Comment on the morphology of the red blood cells.
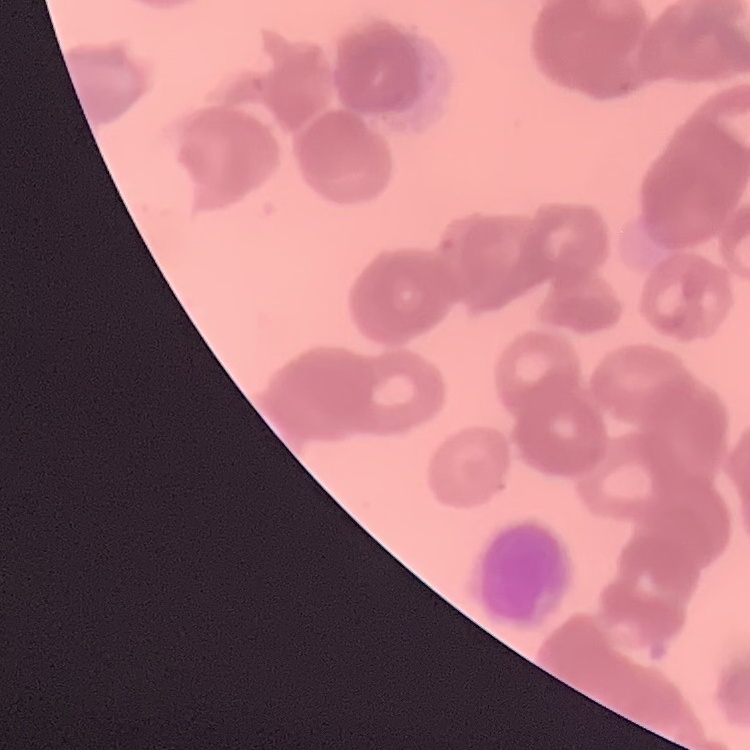

They show rouleaux formation.

Summary:
  - Image type: one tile cut from a larger photomicrograph
  - Stain: Field's or Giemsa
  - Preparation: thin blood film